Give the position of every malaria parasite.
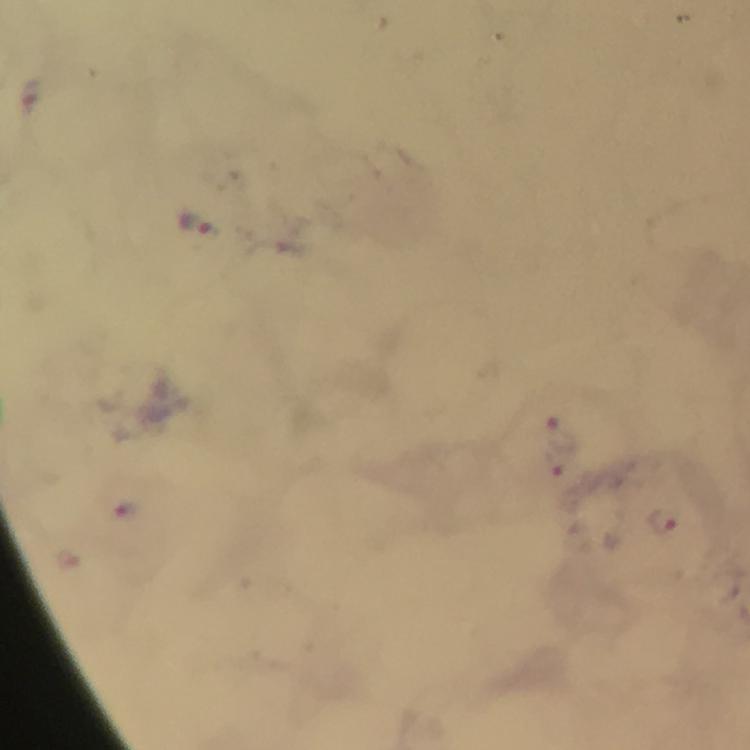
Approximate centers as [x, y] in pixels.
Malaria parasites: [197, 223], [559, 432], [664, 521].

image size = 750×750 pixels
context = from a malaria diagnostic workup
stain = Giemsa
cropped from = a single field of view
capture = smartphone photograph through a microscope
preparation = thick smear
magnification = 100x
immersion oil = used